Report the malaria status.
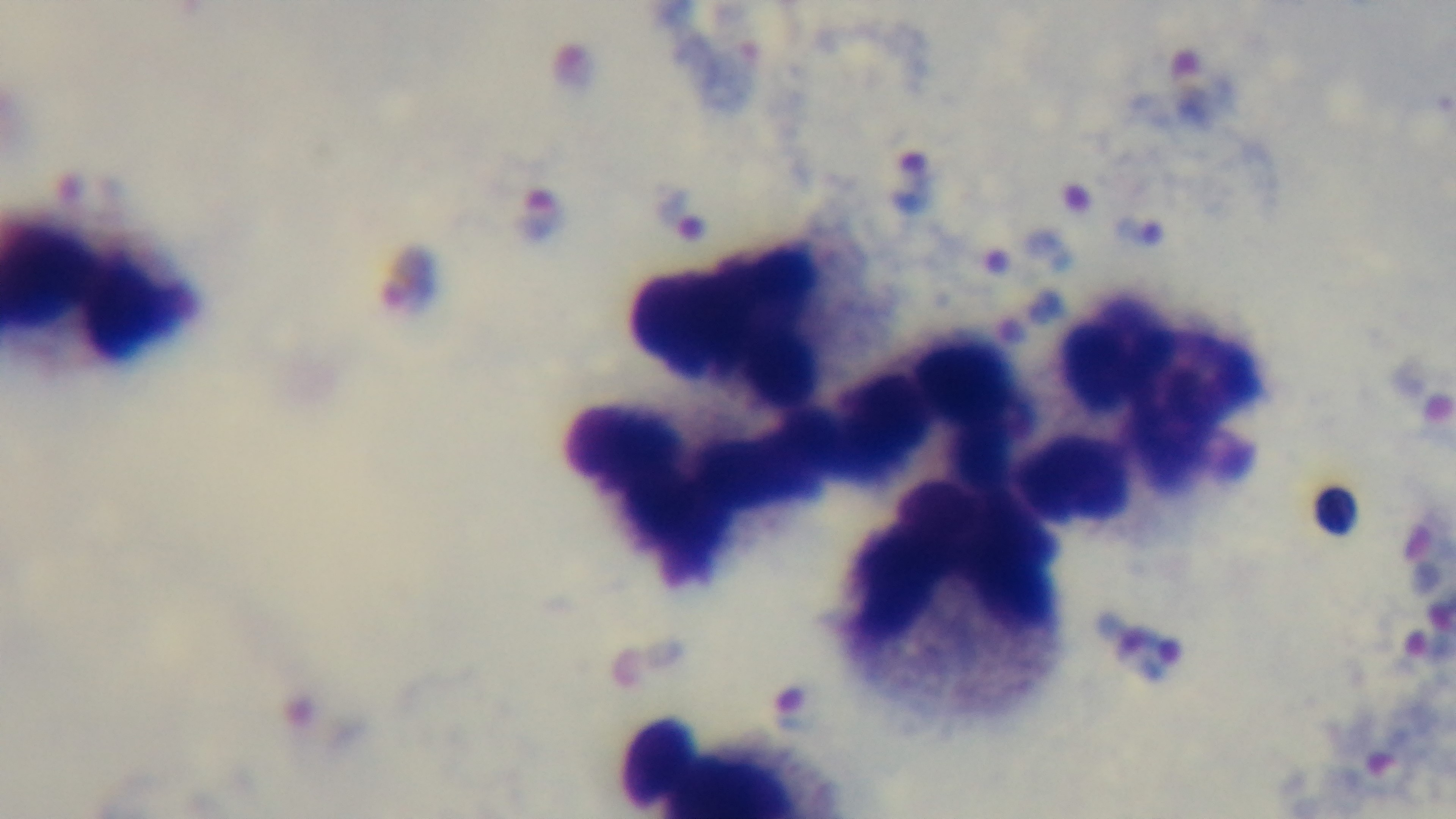

Positive.

Mounted 4K digital camera. Single field of view. Preparation: thick. Giemsa-stained. Photomicrograph. Oil-immersion objective, 100x.